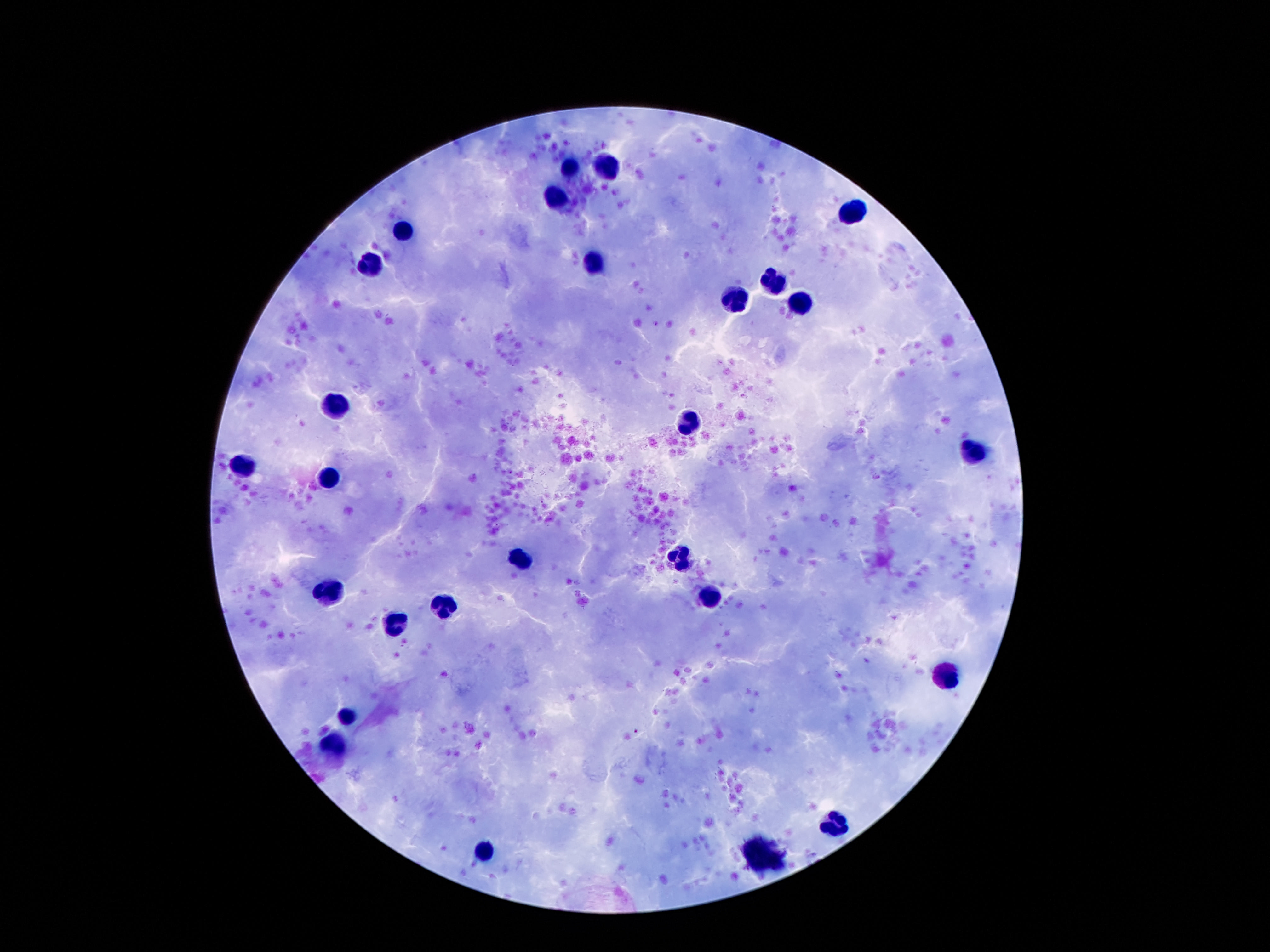

{
  "image_size": "1270×952 pixels",
  "leukocyte_locations": "approximate object centers, in pixels from the top-left corner: (x=571, y=167), (x=608, y=168), (x=556, y=197), (x=853, y=214), (x=404, y=231), (x=367, y=266), (x=596, y=266), (x=774, y=279), (x=735, y=299), (x=801, y=301), (x=337, y=404), (x=689, y=425), (x=973, y=451), (x=244, y=464), (x=326, y=476), (x=522, y=560), (x=681, y=560), (x=326, y=590), (x=447, y=606), (x=396, y=623), (x=942, y=673), (x=346, y=716), (x=333, y=745), (x=835, y=825), (x=487, y=848)",
  "field_of_view": "one from this slide",
  "capture": "smartphone camera through the microscope eyepiece",
  "magnification": "100x",
  "patient_malaria_status": "not infected",
  "preparation": "thick peripheral-blood smear",
  "stain": "Giemsa"
}